Identify the cell.
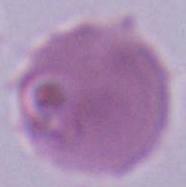
This is an erythrocyte.

{
  "magnification": "1000x",
  "modality": "micrograph"
}